Report the malaria status of this cell.
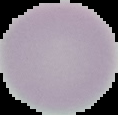

Uninfected.

image type = cell region segmented out of the field of view; surrounding area masked to black
preparation = thin blood film
image size = 118×115 pixels